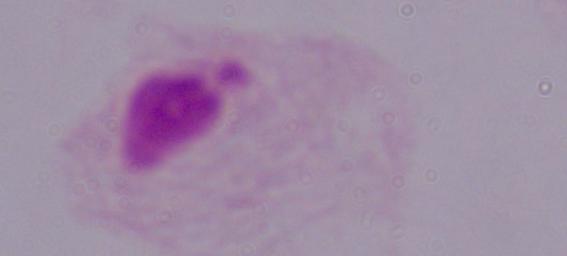
magnification: 1000x
modality: photomicrograph
identification: trichomonad